Assess this cell for malaria.
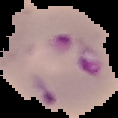

It is parasitized.

Summary:
  - Image size: 118×118 pixels
  - Image type: cell region segmented out of the field of view; surrounding area masked to black
  - Preparation: thin blood smear